Identify the parasite.
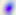

Toxoplasma gondii.

Micrograph. Captured at 400x magnification.